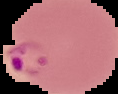
image type = segmented cell region on a black background
malaria status = parasitized
image size = 118×94 pixels
preparation = thin blood smear